Locate and identify every blood parasite.
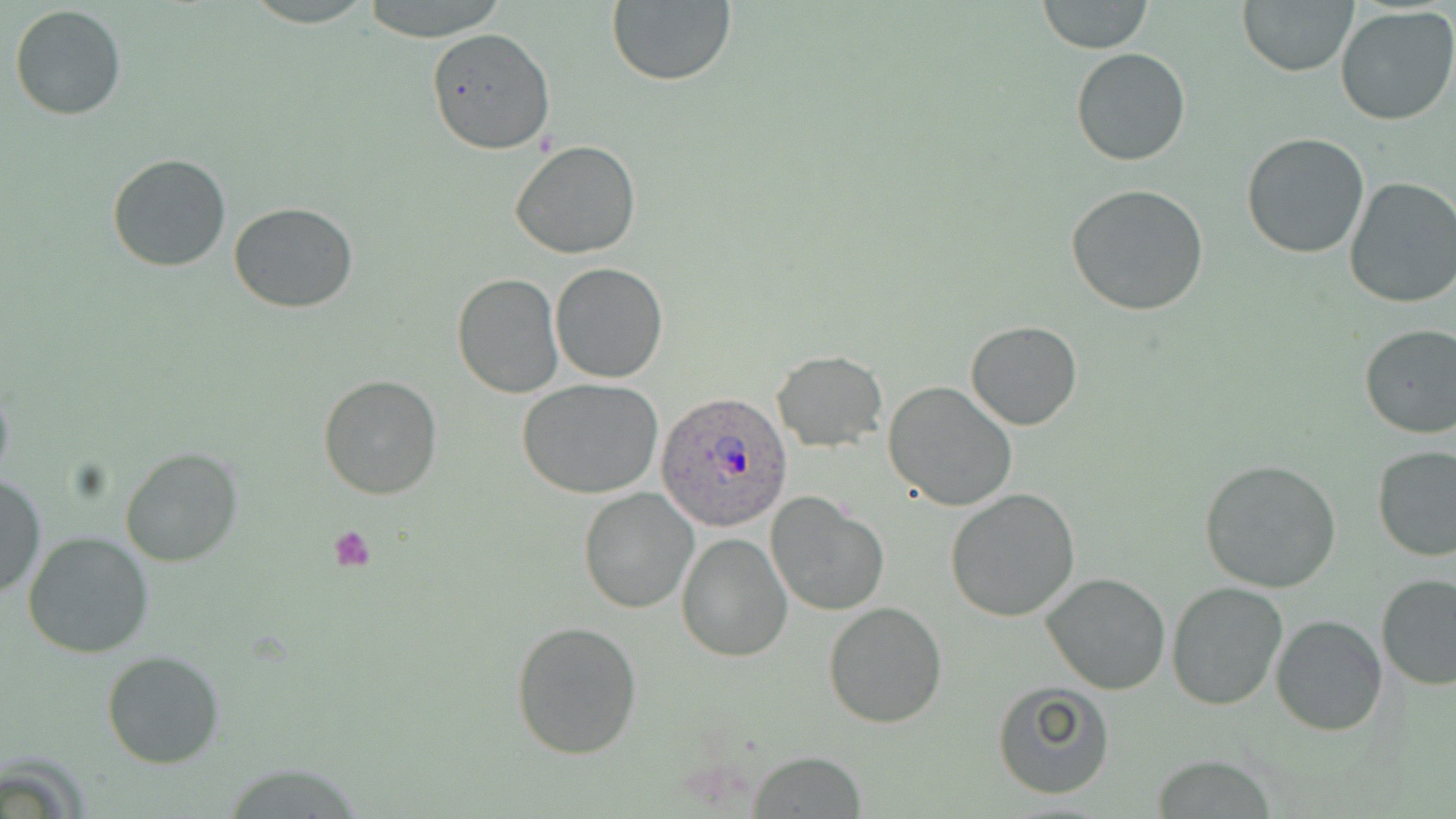
Approximate bounding boxes as (x1,y1)-(x2,y2) corner pairs in pixels.
Plasmodium ovale-infected red blood cells: (655,393)-(796,533).
No Plasmodium falciparum, Plasmodium malariae, Plasmodium vivax, Babesia divergens, or Trypanosoma brucei observed.

Uninfected red blood cell locations: (358,0)-(511,43), (606,1)-(736,87), (1037,1)-(1152,53), (1238,1)-(1357,77), (9,4)-(126,119), (1335,7)-(1456,126), (426,27)-(554,155), (1071,47)-(1191,167), (1241,133)-(1370,259), (509,140)-(642,260), (107,154)-(232,272), (1344,176)-(1456,308), (1066,184)-(1210,317), (229,202)-(359,313), (550,263)-(669,383), (452,272)-(564,397), (967,321)-(1081,431), (1357,323)-(1456,441), (772,350)-(887,452), (318,374)-(442,500), (516,378)-(664,499), (883,380)-(1017,513), (120,447)-(243,568), (1373,447)-(1456,562), (1199,458)-(1343,594), (0,472)-(44,601), (578,486)-(700,614), (944,488)-(1080,622), (766,492)-(889,617), (23,530)-(155,658), (675,532)-(792,663), (1041,571)-(1171,695), (1376,574)-(1456,691), (1165,581)-(1287,710), (822,601)-(948,729), (1271,614)-(1389,736), (510,620)-(643,760), (102,649)-(227,769), (991,681)-(1116,800), (750,751)-(867,817), (1150,757)-(1282,816). Platelet locations: (328,525)-(378,573). Slide-level diagnosis: Plasmodium ovale. Image is 1456×819 pixels. Light microscopy. Single field of view. May-Grünwald-Giemsa-stained preparation. Captured at 1000x magnification. Thin blood smear.